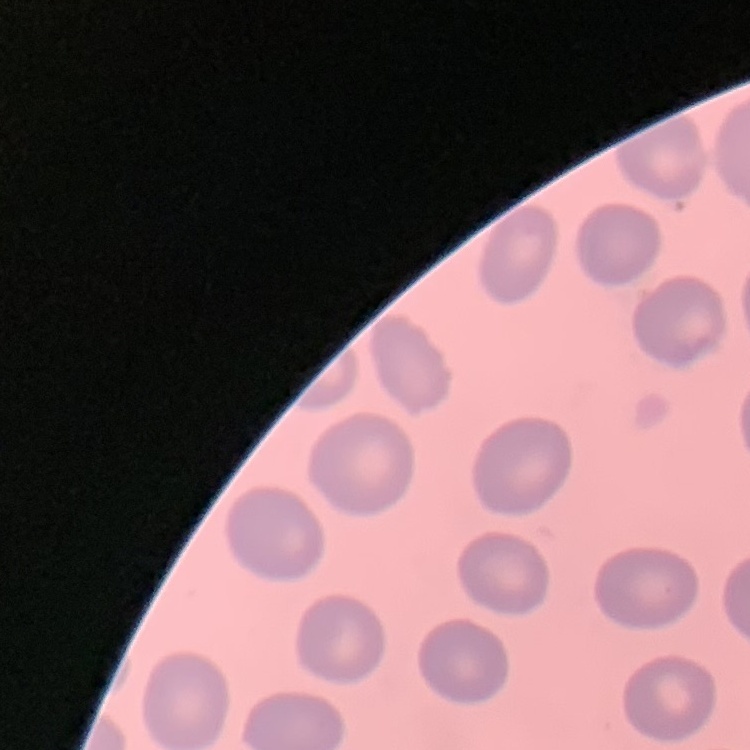

The erythrocytes exhibit no rouleaux formation. Thin peripheral smear. Square crop of a larger photomicrograph. Field's or Giemsa stain.